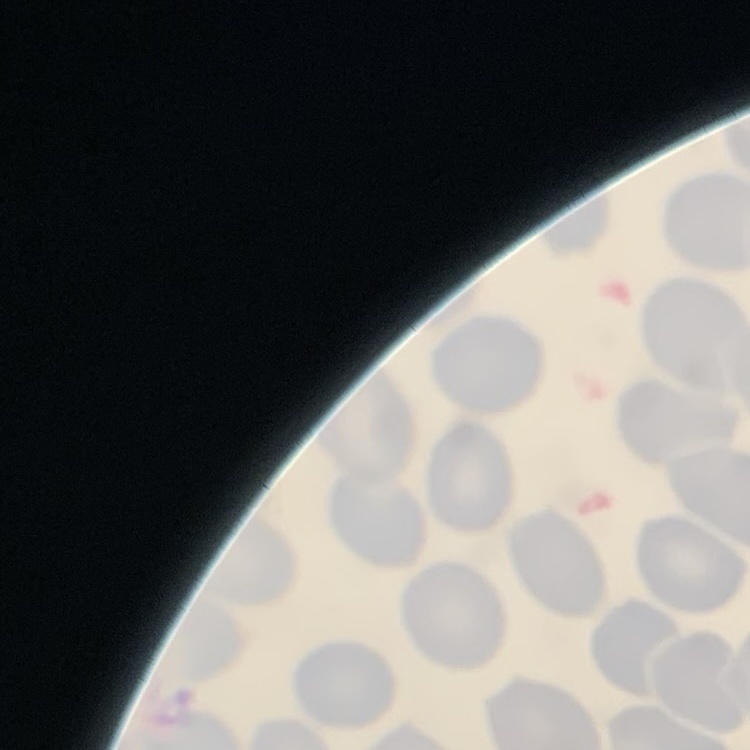
Summary:
  - Red blood cell morphology: no rouleaux formation
  - Stain: Field's or Giemsa
  - Image type: square crop of a larger photomicrograph
  - Preparation: thin blood film